Outline each blood parasite and name the species.
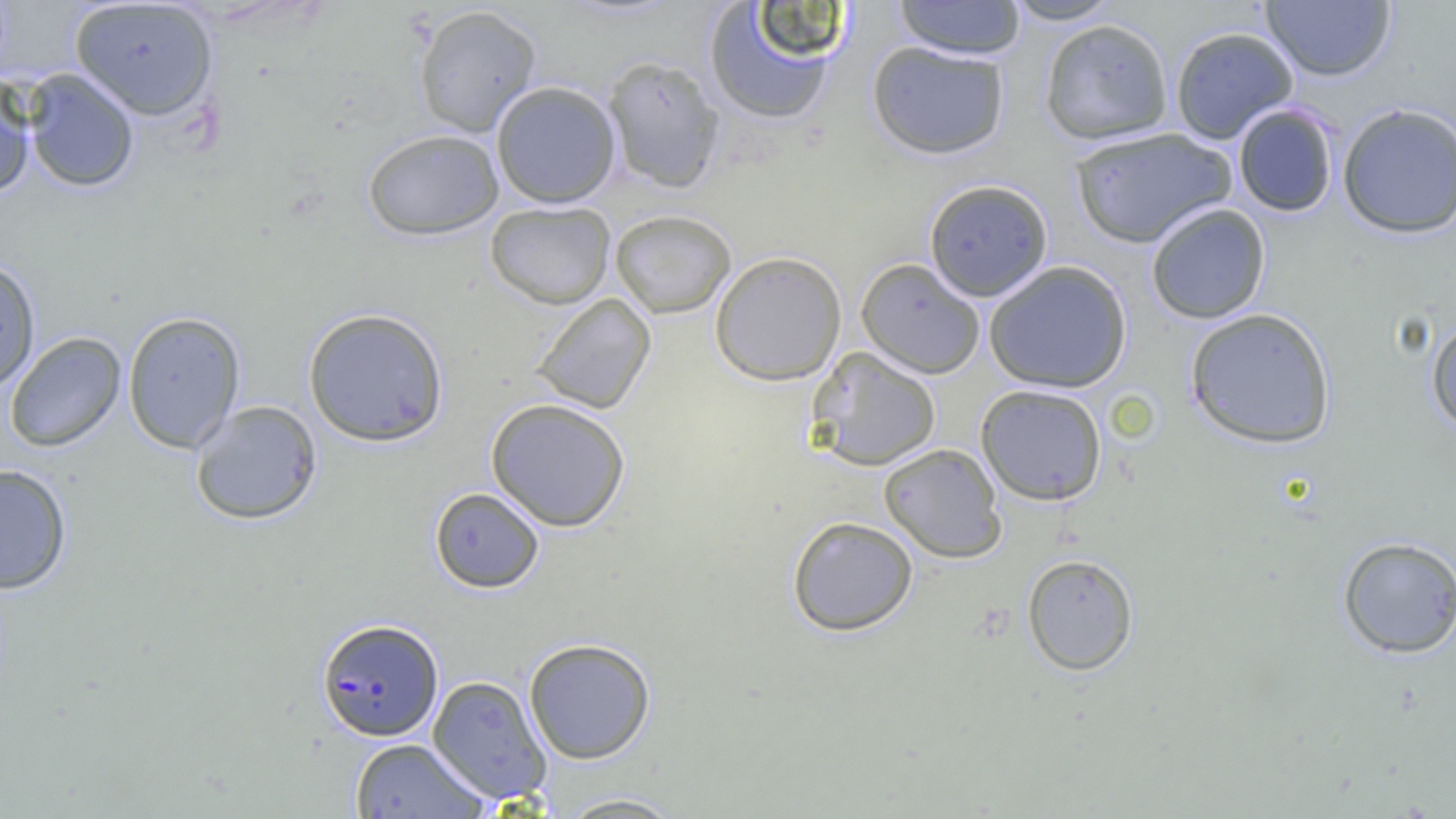
Approximate bounding boxes as [x1, y1, x2, y2] in pixels.
Plasmodium falciparum-infected red blood cells: [316, 618, 443, 741].
No Plasmodium ovale, Plasmodium malariae, Plasmodium vivax, Babesia divergens, or Trypanosoma brucei observed.

Uninfected red blood cell locations: [69, 0, 219, 121], [892, 0, 1027, 59], [1001, 0, 1125, 25], [1260, 1, 1396, 81], [701, 2, 845, 127], [412, 4, 543, 137], [1039, 18, 1174, 144], [1169, 26, 1299, 144], [866, 40, 1010, 159], [602, 55, 725, 193], [22, 68, 140, 193], [0, 75, 36, 200], [491, 80, 622, 208], [1337, 102, 1456, 239], [1233, 104, 1339, 217], [1069, 127, 1236, 249], [362, 128, 504, 240], [923, 178, 1054, 302], [485, 201, 616, 309], [1145, 203, 1271, 325], [609, 209, 737, 318], [709, 250, 847, 385], [0, 257, 41, 393], [855, 258, 986, 379], [984, 260, 1133, 393], [531, 293, 656, 415], [1184, 306, 1337, 449], [303, 307, 449, 447], [122, 311, 246, 454], [1426, 316, 1456, 435], [5, 331, 126, 453], [806, 346, 942, 471], [975, 383, 1108, 506], [485, 398, 631, 532], [190, 400, 323, 525], [879, 443, 1007, 563], [0, 464, 72, 595], [429, 487, 545, 593], [787, 516, 919, 637], [1336, 535, 1456, 658], [1021, 553, 1139, 675], [524, 637, 656, 764], [427, 675, 551, 805], [349, 737, 489, 818], [552, 792, 690, 818]. Slide-level diagnosis: Plasmodium falciparum. One field of a larger specimen. Optical microscopy. Image is 1456×819 pixels. Thin blood smear. Captured at 1000x magnification.